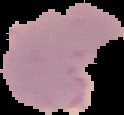 Segmented cell region on a black background. Image is 124×115 pixels. From a thin blood film. Malaria status: parasitized.